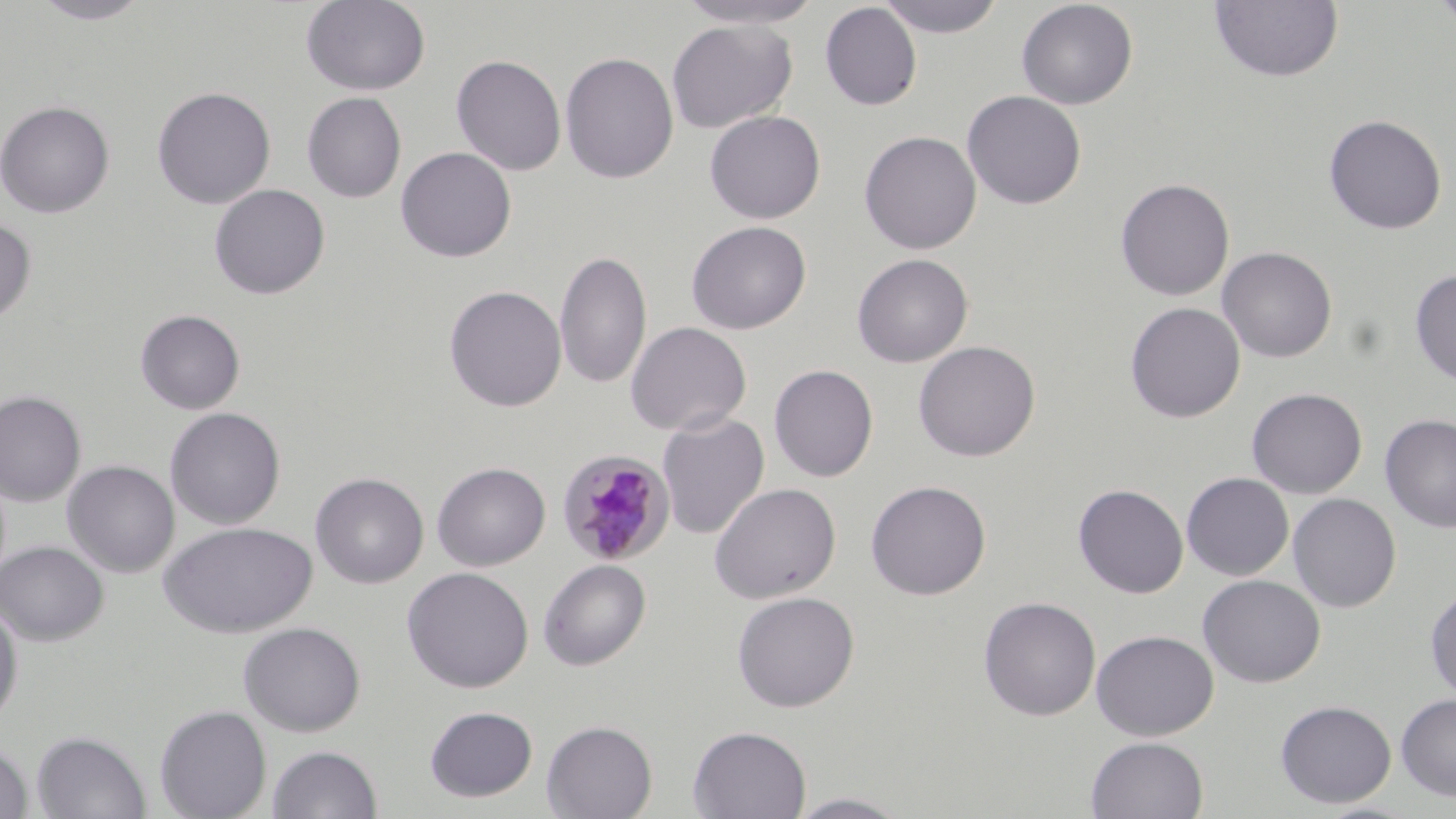
slide-level diagnosis = Plasmodium malariae
magnification = 1000x
stain = May-Grünwald-Giemsa
preparation = thin blood smear
uninfected red blood cell locations = approximate bounding boxes as [x1, y1, x2, y2] in pixels: [27, 0, 156, 24], [301, 0, 430, 96], [675, 0, 827, 28], [876, 0, 1007, 38], [1016, 0, 1138, 110], [1208, 0, 1344, 83], [1431, 0, 1456, 32], [820, 2, 922, 111], [666, 19, 797, 134], [560, 51, 679, 184], [450, 54, 567, 176], [152, 85, 276, 209], [962, 90, 1087, 210], [302, 92, 406, 203], [0, 99, 116, 218], [704, 110, 826, 224], [1323, 114, 1447, 235], [859, 130, 982, 254], [395, 146, 517, 263], [1115, 177, 1235, 301], [209, 184, 330, 300], [0, 218, 36, 325], [686, 220, 811, 334], [1217, 246, 1338, 363], [554, 249, 653, 390], [852, 253, 973, 368], [1410, 267, 1456, 387], [444, 285, 567, 412], [1125, 301, 1245, 423], [134, 308, 246, 415], [626, 321, 752, 437], [913, 340, 1040, 462], [769, 364, 878, 482], [1246, 387, 1367, 499], [0, 390, 86, 507], [165, 407, 286, 530], [657, 412, 769, 539], [1380, 413, 1456, 533], [62, 460, 180, 578], [432, 461, 550, 571], [311, 472, 429, 588], [1181, 472, 1294, 581], [865, 480, 991, 600], [709, 482, 841, 604], [1073, 483, 1189, 599], [1288, 493, 1401, 612], [159, 521, 317, 638], [0, 540, 108, 646], [538, 559, 651, 671], [401, 566, 534, 693], [1198, 574, 1326, 688], [1425, 586, 1456, 703], [732, 590, 860, 712], [978, 596, 1101, 721], [0, 601, 24, 729], [238, 621, 366, 737], [1091, 629, 1219, 741], [1396, 693, 1456, 801], [1275, 700, 1397, 808], [155, 705, 272, 819], [424, 706, 538, 802], [542, 719, 657, 819], [688, 725, 812, 819], [32, 730, 151, 819], [1086, 735, 1209, 818], [0, 740, 33, 819], [267, 744, 383, 819], [785, 791, 913, 818]
field of view = single
Plasmodium malariae-infected red blood cell locations = approximate bounding boxes as [x1, y1, x2, y2] in pixels: [556, 449, 675, 565]
image size = 1456×819 pixels
modality = optical microscopy